Report the malaria status of this cell.
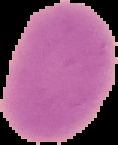

It is uninfected.

image type = cell region segmented out of the field of view; surrounding area masked to black
image size = 118×145 pixels
preparation = thin blood smear